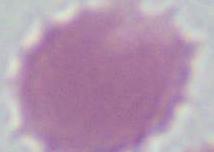
{
  "modality": "photomicrograph",
  "magnification": "1000x",
  "identification": "red blood cell"
}